State the preparation type.
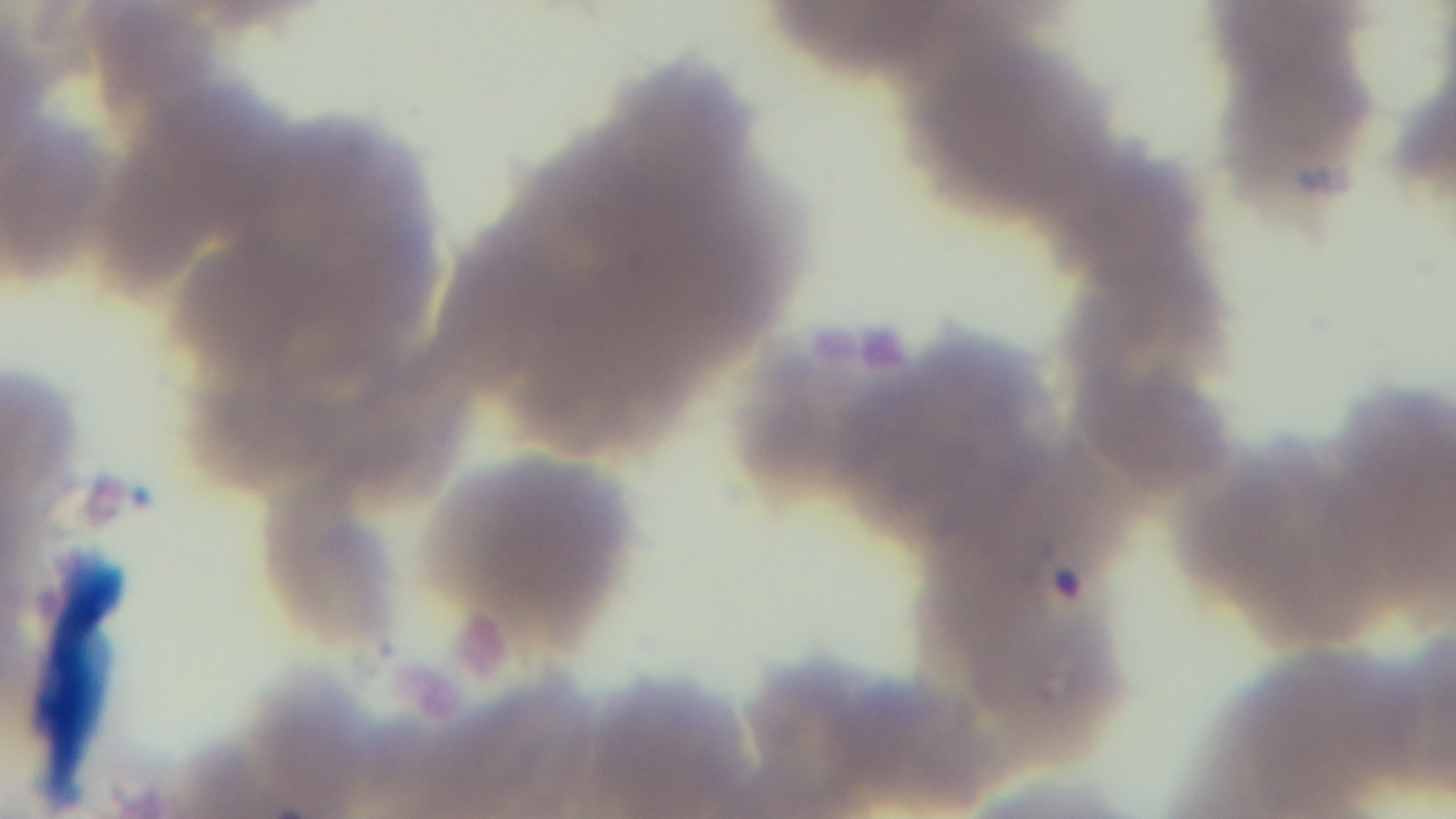
It is a thin blood film.

malaria_status: infected
field_of_view: single
stain: Giemsa
modality: light microscopy
capture: mounted 4K digital camera
objective: 100x oil immersion